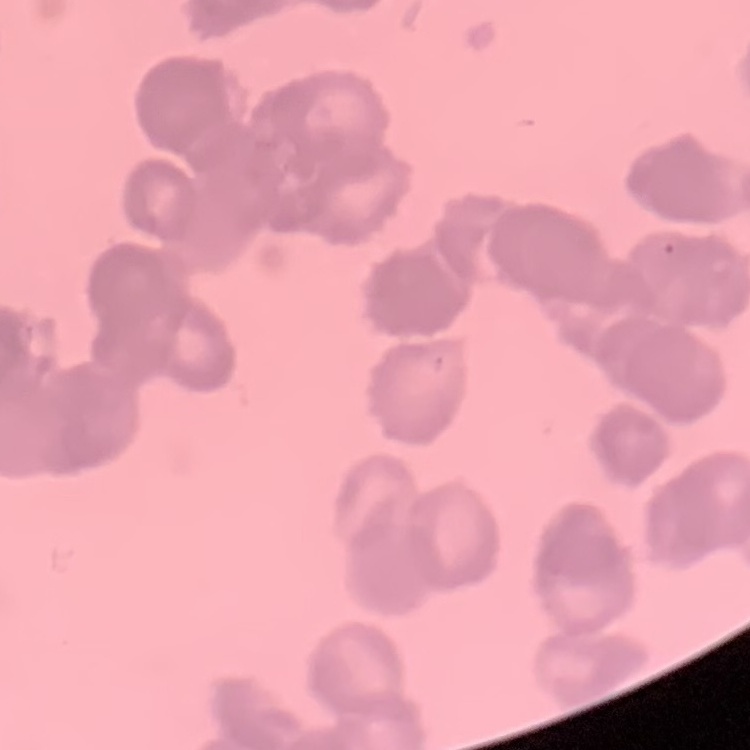
Summary:
  - Red blood cell morphology: rouleaux formation
  - Image type: one tile cut from a larger photomicrograph
  - Preparation: thin blood film
  - Stain: Field's or Giemsa